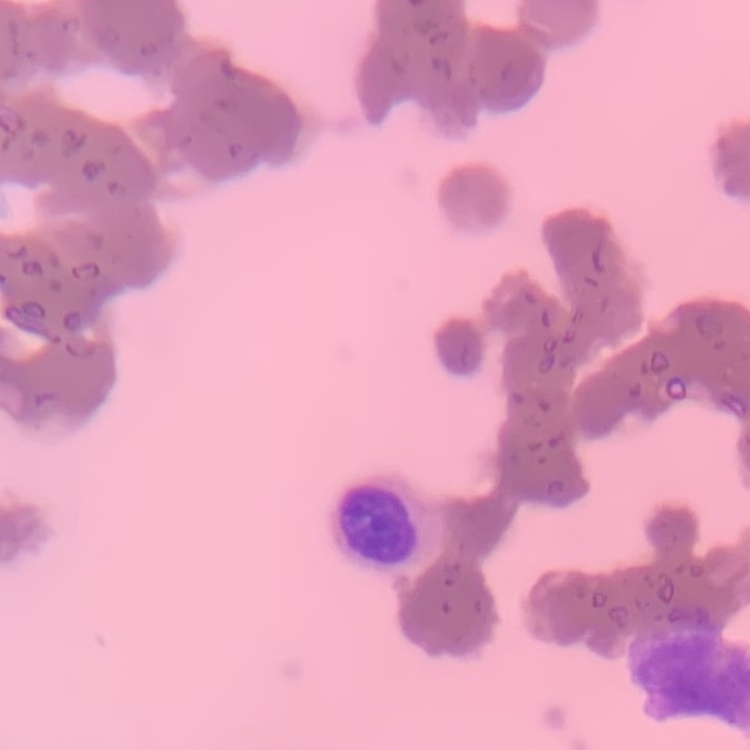

Summary:
  - Red blood cell morphology: rouleaux formation
  - Stain: Field's or Giemsa
  - Preparation: thin blood smear
  - Image type: square crop of a larger photomicrograph